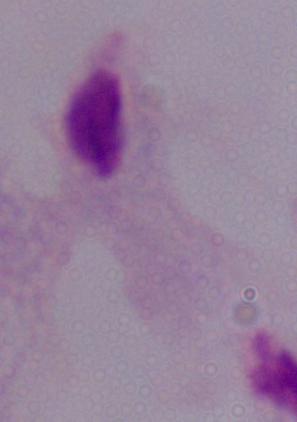

A trichomonad is shown. Captured at 1000x magnification. Photomicrograph.